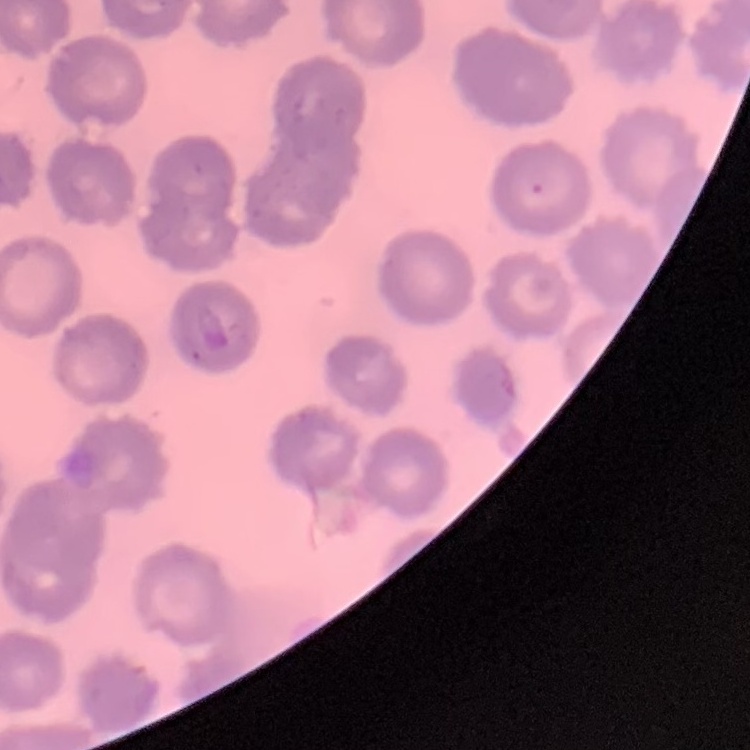
Summary:
  - Red blood cell morphology: no rouleaux formation
  - Stain: Field's or Giemsa
  - Image type: one tile cut from a larger photomicrograph
  - Preparation: thin peripheral smear